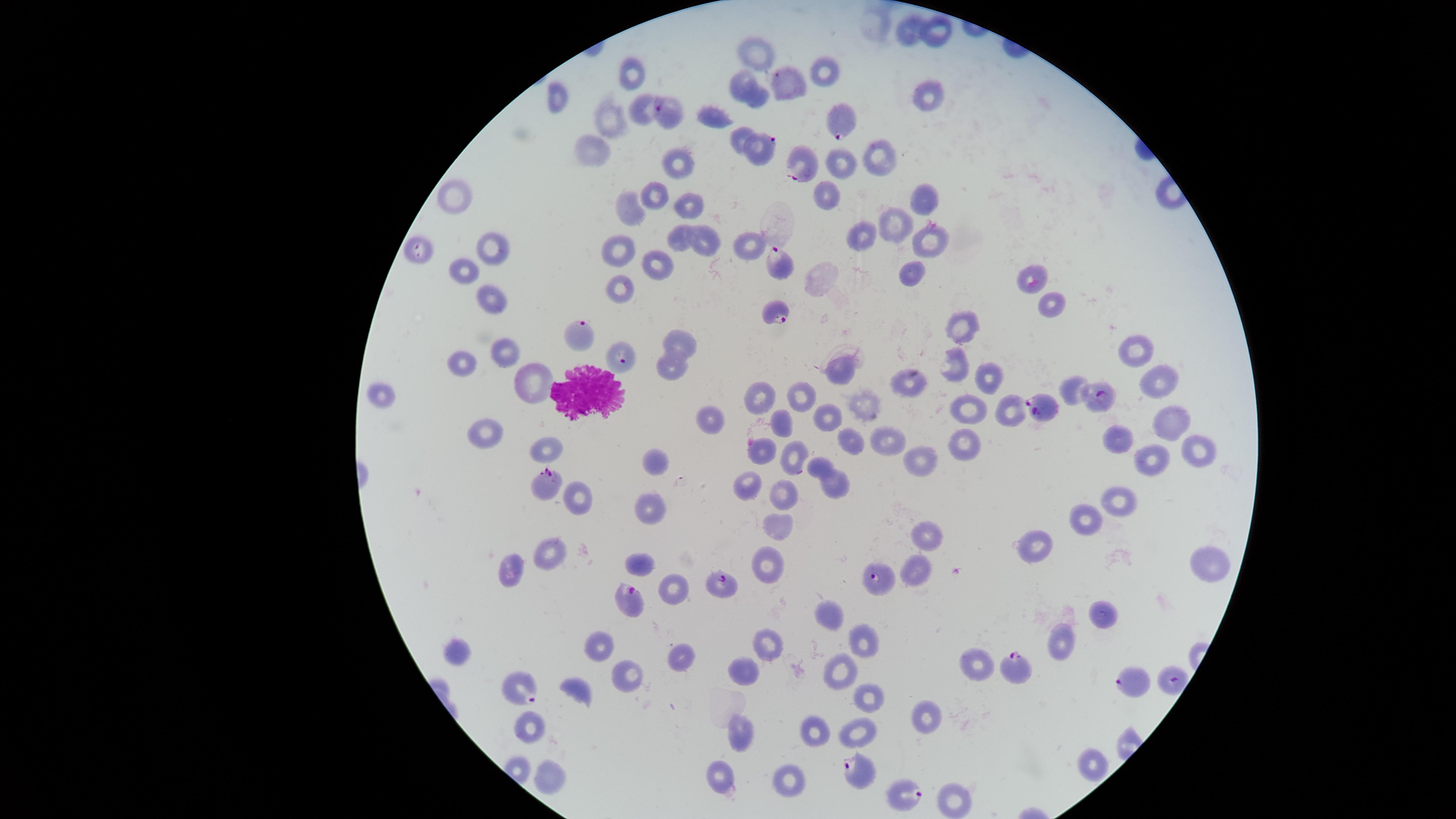
{
  "presence": "malaria parasites seen",
  "image_size": "1456×819 pixels",
  "field_of_view": "single",
  "species": "Plasmodium falciparum",
  "uninfected_RBCs": "approximate marker points as [x, y] in pixels: [913, 30], [938, 32], [752, 54], [631, 71], [827, 71], [739, 82], [560, 96], [930, 96], [758, 98], [642, 111], [718, 116], [609, 118], [739, 136], [596, 146], [880, 156], [680, 163], [448, 195], [658, 195], [925, 197], [629, 208], [692, 208], [897, 218], [862, 234], [678, 237], [745, 240], [928, 240], [497, 242], [703, 245], [620, 248], [658, 263], [468, 268], [912, 269], [1032, 279], [622, 283], [496, 297], [1051, 304], [964, 323], [683, 338], [506, 350], [1135, 350], [463, 361], [955, 366], [670, 367], [839, 369], [985, 376], [1160, 380], [528, 383], [911, 383], [1067, 385], [378, 393], [761, 395], [802, 396], [862, 404], [970, 410], [1009, 410], [708, 417], [829, 418], [1173, 418], [782, 419], [492, 428], [1117, 435], [883, 438], [848, 440], [960, 446], [758, 449], [1195, 451], [553, 452], [922, 454], [799, 456], [1155, 456], [655, 459], [817, 470], [749, 481], [837, 483], [784, 488], [578, 495], [1123, 497], [650, 508], [1086, 520], [779, 529], [928, 536], [1039, 546], [548, 556], [1206, 563], [641, 565], [769, 565], [514, 571], [916, 572], [672, 590], [1105, 610], [832, 614], [867, 638], [767, 642], [1063, 644], [456, 651], [599, 651], [679, 658], [979, 664], [743, 668], [840, 671], [624, 681], [576, 692], [869, 692], [929, 718], [533, 728], [739, 728], [856, 728], [818, 730], [1089, 767], [548, 776], [786, 778], [716, 780], [953, 801]",
  "capture": "smartphone photograph through the microscope eyepiece",
  "stain": "Giemsa",
  "parasitized_RBCs": "approximate marker points as [x, y] in pixels: [787, 83], [670, 112], [844, 121], [764, 151], [799, 167], [419, 250], [783, 267], [776, 310], [581, 339], [621, 363], [1099, 397], [1044, 406], [551, 479], [882, 580], [726, 586], [633, 601], [1014, 664], [1174, 677], [521, 682], [1135, 683], [855, 767], [900, 790]",
  "WBCs": "approximate marker points as [x, y] in pixels: [587, 392]",
  "visible_region": "circular",
  "preparation": "thin blood film"
}